Locate every blood parasite and identify its species.
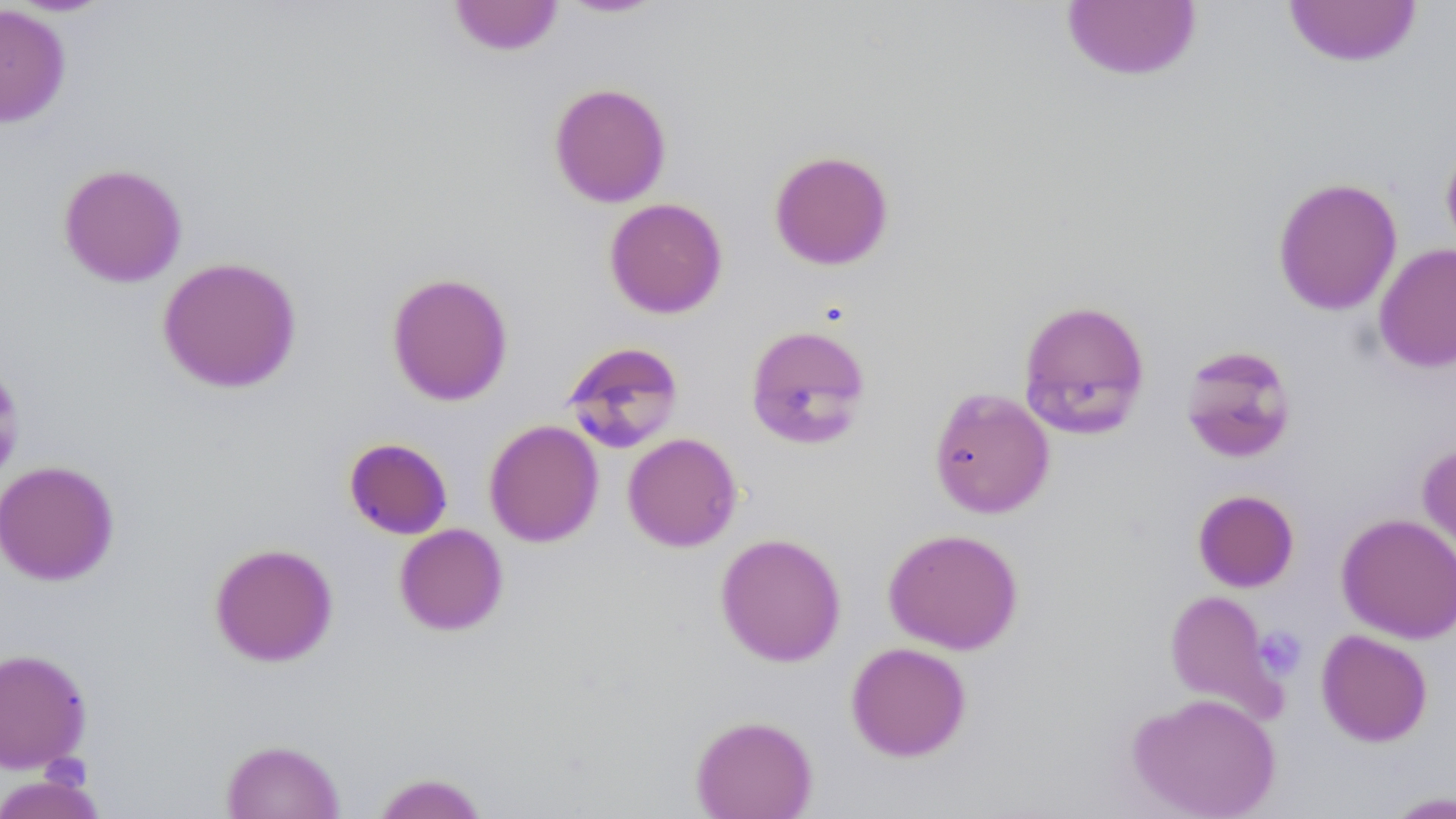
No blood parasites seen.

Summary:
  - Coordinate format: approximate bounding boxes as named x1/y1/x2/y2 corners in pixels
  - Uninfected red blood cell locations: (x1=447, y1=0, x2=564, y2=56), (x1=556, y1=0, x2=667, y2=19), (x1=1060, y1=1, x2=1202, y2=82), (x1=1282, y1=1, x2=1423, y2=68), (x1=0, y1=5, x2=71, y2=128), (x1=548, y1=82, x2=672, y2=208), (x1=1440, y1=139, x2=1456, y2=260), (x1=768, y1=150, x2=894, y2=271), (x1=57, y1=162, x2=188, y2=288), (x1=1272, y1=177, x2=1403, y2=316), (x1=604, y1=197, x2=728, y2=319), (x1=1374, y1=243, x2=1456, y2=373), (x1=157, y1=256, x2=302, y2=394), (x1=386, y1=271, x2=514, y2=406), (x1=1017, y1=298, x2=1151, y2=440), (x1=744, y1=324, x2=873, y2=451), (x1=561, y1=340, x2=685, y2=454), (x1=1179, y1=344, x2=1298, y2=463), (x1=928, y1=387, x2=1055, y2=519), (x1=484, y1=419, x2=604, y2=547), (x1=622, y1=432, x2=742, y2=552), (x1=343, y1=437, x2=453, y2=540), (x1=1417, y1=439, x2=1456, y2=571), (x1=0, y1=460, x2=120, y2=586), (x1=1192, y1=489, x2=1300, y2=592), (x1=1336, y1=512, x2=1456, y2=643), (x1=394, y1=523, x2=508, y2=636), (x1=882, y1=528, x2=1024, y2=654), (x1=714, y1=532, x2=847, y2=667), (x1=208, y1=542, x2=339, y2=667), (x1=1163, y1=589, x2=1287, y2=723), (x1=1316, y1=629, x2=1433, y2=747), (x1=845, y1=641, x2=972, y2=762), (x1=0, y1=647, x2=92, y2=774), (x1=1127, y1=692, x2=1281, y2=818), (x1=690, y1=714, x2=818, y2=818), (x1=220, y1=739, x2=345, y2=819), (x1=0, y1=771, x2=107, y2=819), (x1=369, y1=772, x2=490, y2=818), (x1=1380, y1=790, x2=1456, y2=819)
  - Platelet locations: (x1=1253, y1=626, x2=1308, y2=680)
  - Slide-level diagnosis: no evidence of blood parasites
  - Preparation: thin blood film
  - Stain: May-Grünwald-Giemsa
  - Modality: optical microscopy
  - Magnification: 1000x
  - Image size: 1456×819 pixels
  - Field of view: one of a larger specimen